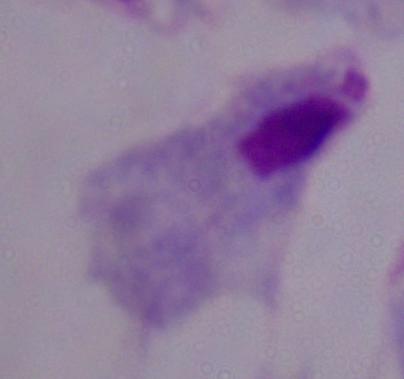

Summary:
  - Magnification: 1000x
  - Identification: trichomonad
  - Modality: micrograph